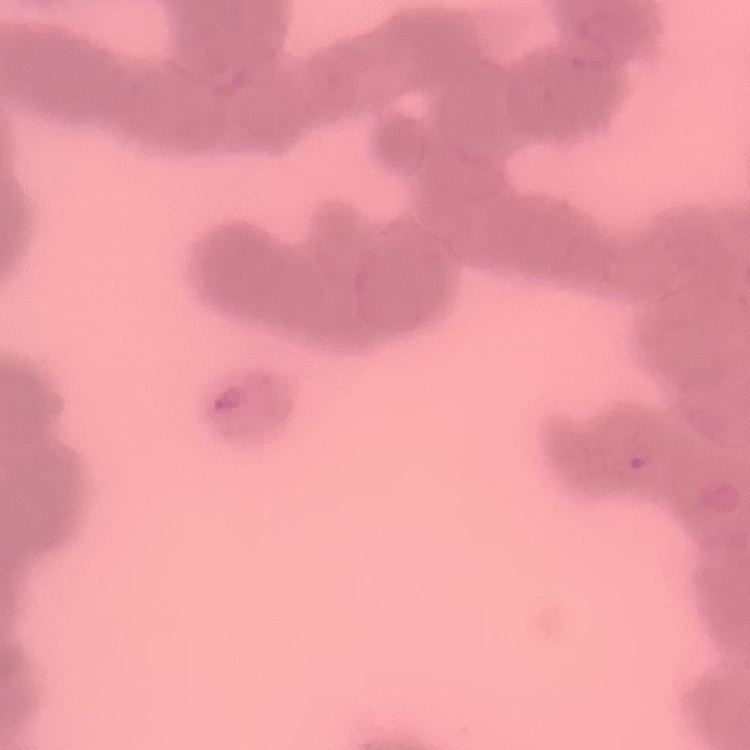 The erythrocytes show rouleaux formation. Square crop of a larger photomicrograph. Stained with either Field's or Giemsa. Thin blood film.